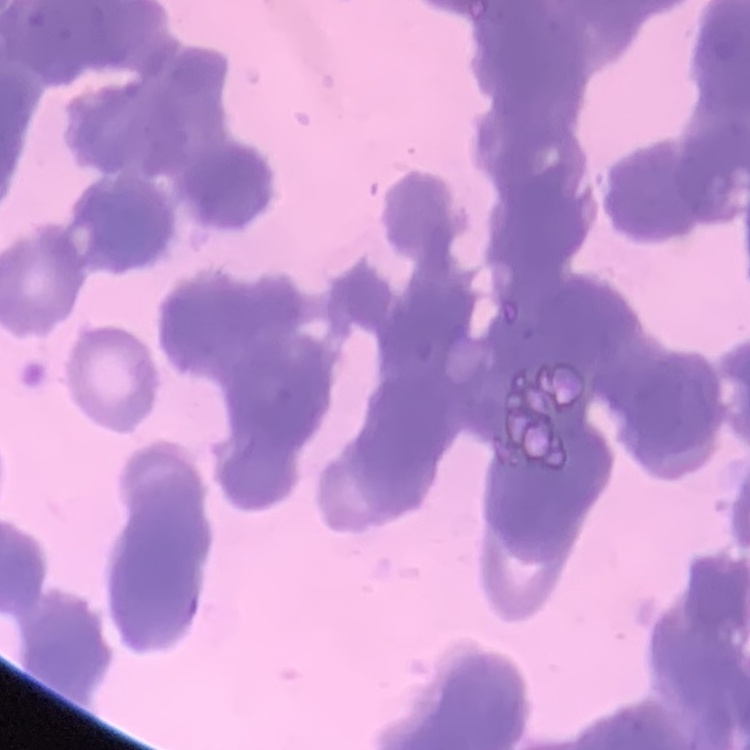
Summary:
  - Erythrocyte morphology: rouleaux formation
  - Preparation: thin blood film
  - Stain: Field's or Giemsa
  - Image type: square crop of a larger photomicrograph